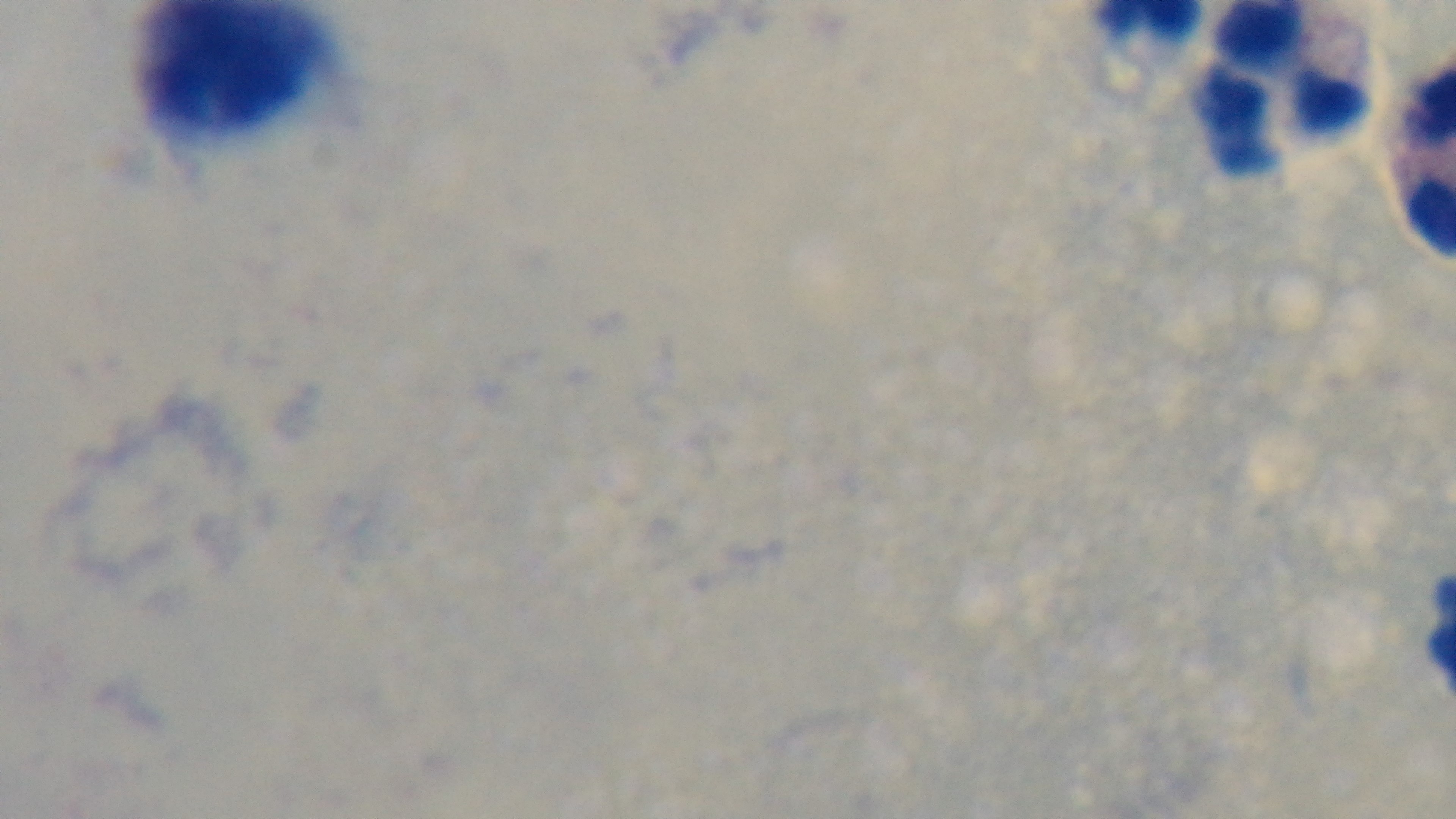
Summary:
  - Capture: mounted 4K digital camera
  - Malaria status: negative
  - Objective: 100x oil immersion
  - Preparation: thick blood film
  - Stain: Giemsa
  - Field of view: single
  - Modality: light microscopy